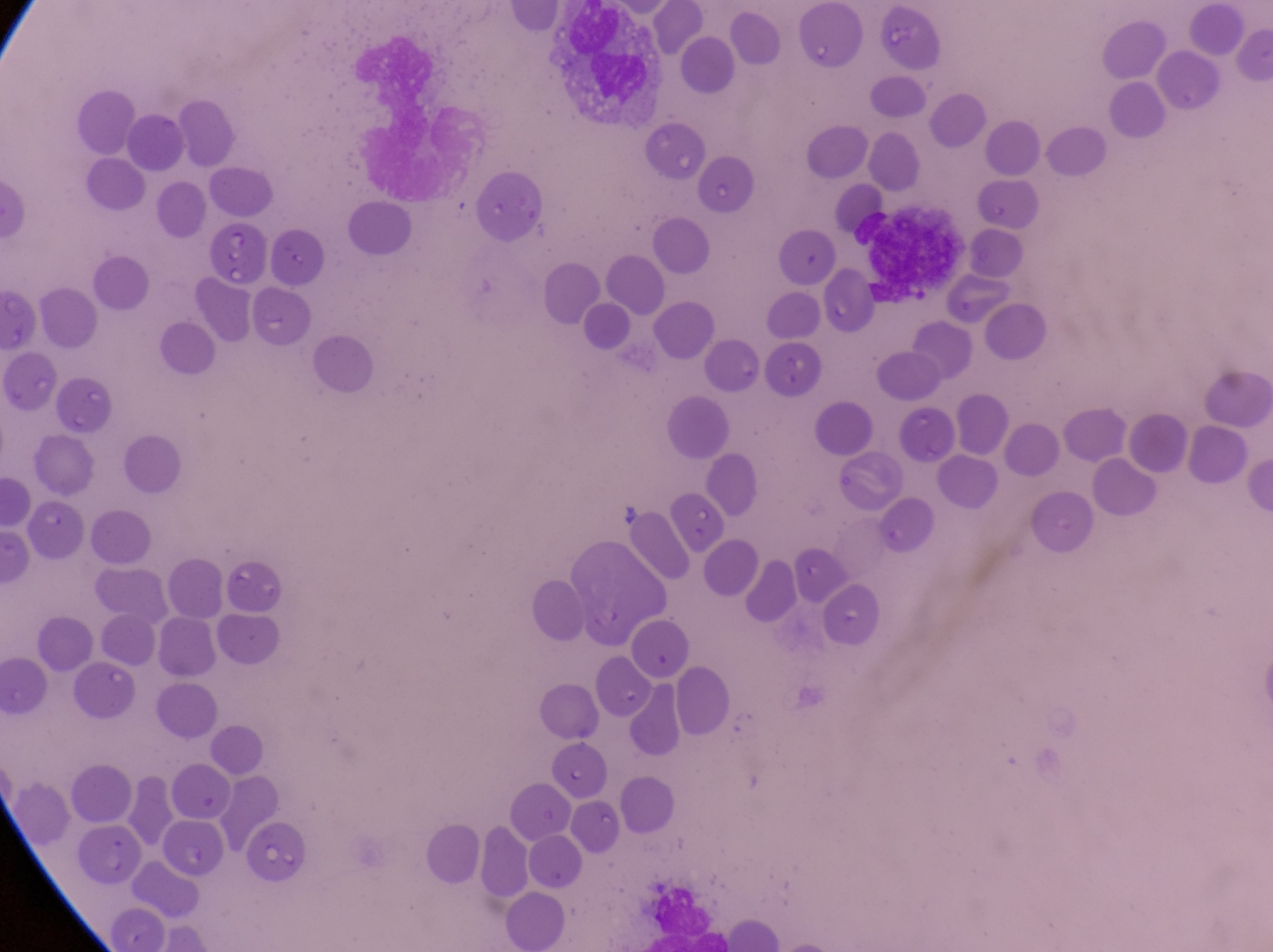
Approximate bounding boxes as left top right bottom in pixels.
Summary:
  - Parasitised red blood cell locations: 210 223 263 291; 821 270 874 340; 244 827 311 880
  - Leukocyte locations: 554 13 662 118
  - Capture: smartphone photograph through the eyepiece of an Olympus CX-23 microscope
  - Country: Uganda
  - Preparation: thin blood film
  - Image size: 1273×952 pixels
  - Magnification: 1000x
  - Field of view: single